Classify this cell by malaria status.
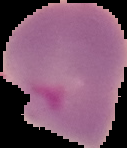

Parasitized.

Summary:
  - Image type: segmented cell region on a black background
  - Image size: 127×148 pixels
  - Preparation: thin blood smear